Locate and identify every blood parasite.
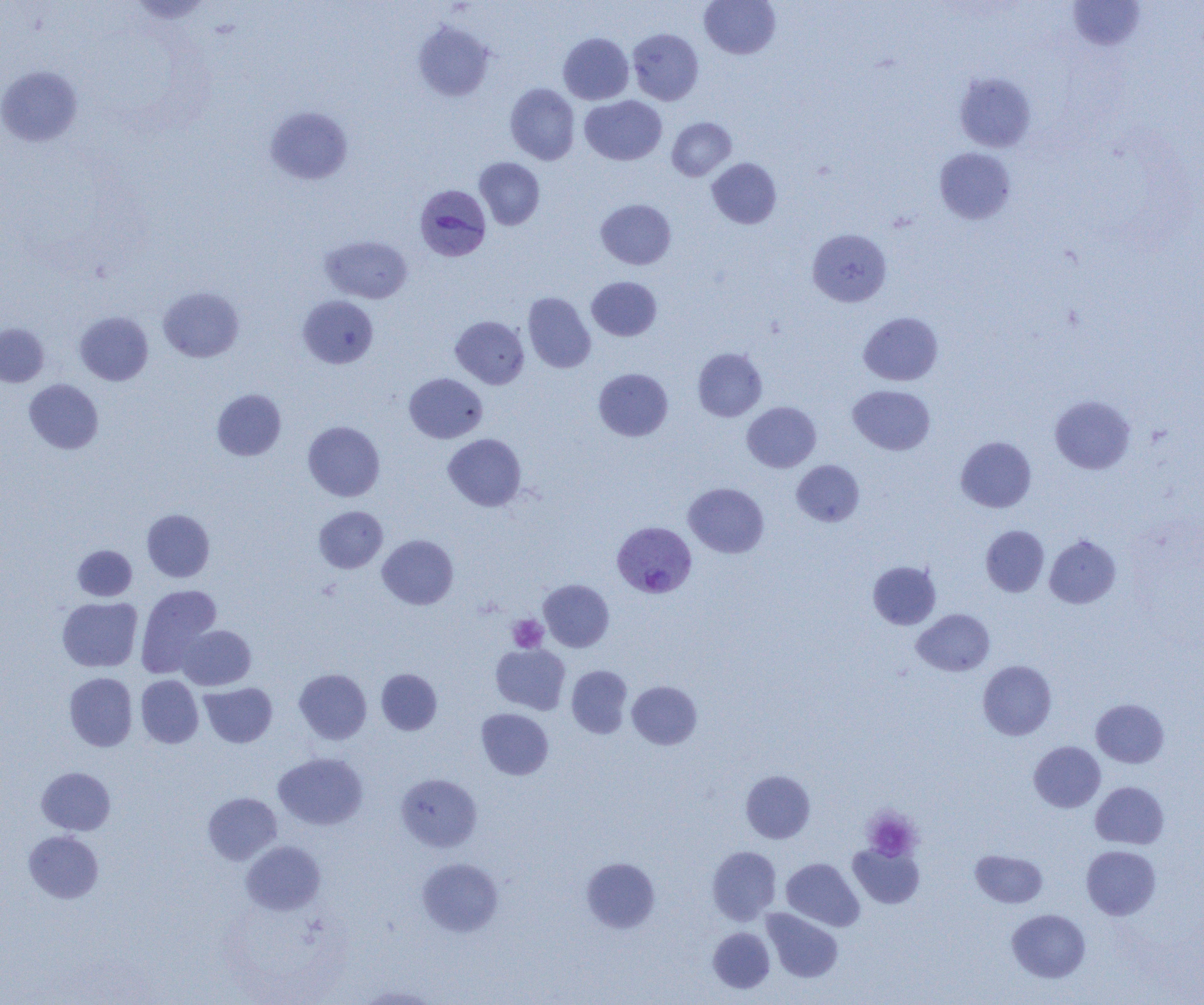
Approximate bounding boxes as [x1, y1, x2, y2] in pixels.
Plasmodium vivax-infected red blood cells: [414, 184, 491, 261], [612, 524, 697, 601].
No Plasmodium falciparum, Plasmodium ovale, Plasmodium malariae, Babesia divergens, or Trypanosoma brucei observed.

Summary:
  - Platelet locations: [507, 614, 548, 652], [862, 807, 921, 861]
  - Uninfected red blood cell locations: [699, 0, 781, 59], [1067, 0, 1147, 51], [414, 21, 494, 101], [628, 28, 704, 105], [558, 33, 634, 104], [0, 66, 83, 146], [954, 73, 1036, 152], [505, 83, 580, 165], [580, 95, 666, 165], [265, 106, 353, 184], [667, 117, 736, 181], [934, 148, 1016, 224], [474, 157, 545, 230], [707, 158, 781, 229], [596, 199, 676, 270], [807, 228, 891, 307], [320, 235, 413, 303], [587, 277, 662, 341], [158, 287, 244, 362], [523, 292, 595, 373], [298, 295, 378, 368], [75, 311, 153, 385], [858, 312, 943, 385], [451, 316, 529, 388], [0, 323, 49, 387], [693, 348, 767, 421], [593, 368, 673, 441], [404, 373, 488, 443], [24, 379, 104, 454], [848, 385, 935, 455], [212, 389, 286, 461], [1049, 395, 1135, 474], [742, 402, 821, 472], [303, 421, 385, 502], [443, 434, 526, 511], [956, 437, 1036, 512], [791, 460, 865, 527], [683, 482, 769, 558], [314, 506, 388, 573], [142, 509, 214, 582], [981, 525, 1049, 596], [378, 534, 458, 609], [1045, 535, 1120, 608], [72, 545, 137, 601], [868, 561, 941, 629], [538, 579, 614, 652], [135, 584, 222, 678], [57, 597, 142, 672], [912, 609, 995, 676], [177, 625, 256, 690], [491, 644, 570, 714], [978, 660, 1056, 740], [567, 665, 633, 738], [294, 668, 372, 744], [376, 668, 442, 735], [64, 672, 137, 751], [136, 675, 203, 748], [627, 681, 702, 750], [200, 683, 277, 747], [1091, 698, 1169, 767], [476, 708, 553, 780], [1028, 741, 1105, 812], [274, 752, 368, 831], [36, 767, 115, 835], [740, 770, 815, 843], [396, 773, 482, 852], [1090, 782, 1169, 849], [203, 792, 282, 865], [24, 831, 104, 903], [241, 841, 325, 915], [848, 842, 925, 909], [1081, 845, 1161, 920], [707, 846, 781, 925], [970, 849, 1048, 908], [417, 857, 503, 937], [581, 857, 660, 933], [781, 858, 864, 931], [762, 908, 843, 982], [1007, 909, 1090, 982], [708, 927, 775, 993], [355, 984, 442, 1004]
  - Slide-level diagnosis: Plasmodium vivax
  - Field of view: one of a larger specimen
  - Image size: 1204×1005 pixels
  - Magnification: 1000x
  - Preparation: thin blood film
  - Modality: light microscopy